Classify this cell by malaria status.
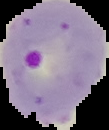

It is parasitized.

Summary:
  - Preparation: thin blood film
  - Image type: segmented cell region on a black background
  - Image size: 109×130 pixels